Outline each Plasmodium malariae-infected red blood cell.
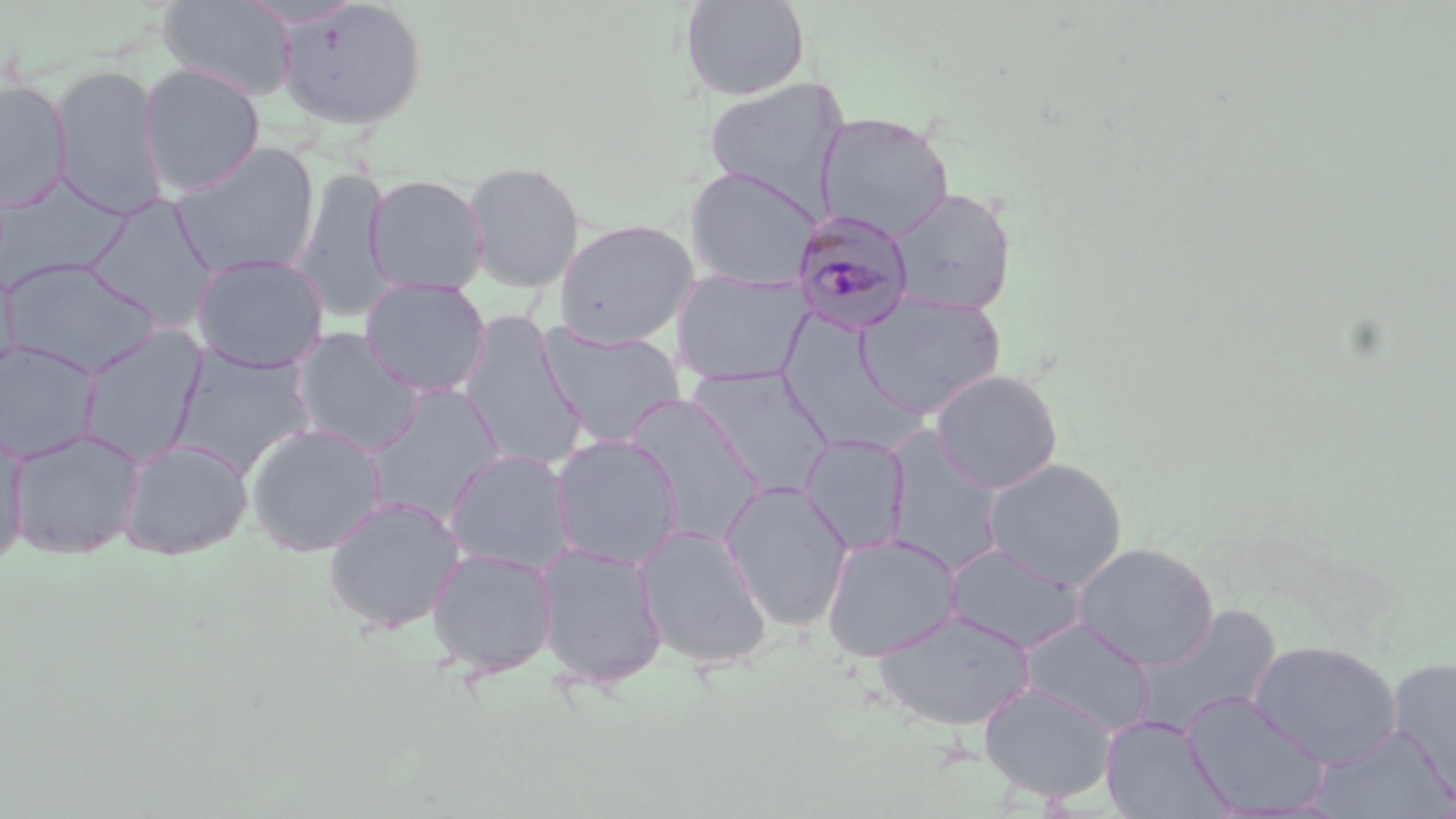
Approximate bounding boxes as [x1, y1, x2, y2] in pixels.
Plasmodium malariae-infected red blood cells: [790, 208, 916, 335].

Uninfected red blood cell locations: [158, 0, 296, 101], [276, 0, 428, 130], [680, 0, 810, 101], [138, 62, 265, 196], [50, 63, 168, 220], [0, 79, 72, 211], [702, 79, 849, 208], [815, 112, 954, 239], [170, 142, 321, 279], [462, 160, 586, 292], [684, 167, 822, 290], [293, 168, 395, 322], [365, 173, 489, 294], [0, 176, 129, 291], [887, 187, 1018, 317], [84, 194, 219, 330], [554, 219, 699, 349], [191, 253, 329, 373], [1, 257, 160, 376], [0, 262, 22, 383], [670, 267, 812, 388], [359, 278, 492, 397], [854, 291, 1005, 420], [458, 314, 589, 470], [538, 323, 686, 447], [77, 325, 207, 467], [290, 328, 425, 455], [0, 340, 102, 464], [170, 346, 316, 477], [687, 367, 835, 498], [930, 369, 1063, 493], [364, 386, 508, 522], [622, 393, 767, 544], [0, 422, 29, 565], [245, 422, 387, 557], [882, 427, 1006, 574], [7, 428, 144, 559], [551, 434, 684, 570], [800, 434, 911, 556], [118, 438, 253, 559], [444, 449, 576, 575], [982, 457, 1127, 590], [719, 481, 854, 629], [323, 495, 465, 634], [634, 524, 772, 669], [821, 532, 962, 662], [535, 540, 669, 690], [945, 542, 1086, 653], [1072, 543, 1219, 670], [426, 548, 558, 678], [1130, 605, 1282, 738], [873, 609, 1035, 732], [1019, 618, 1155, 736], [1248, 640, 1402, 767], [1387, 659, 1456, 797], [978, 681, 1117, 804], [1181, 691, 1331, 816], [1100, 715, 1230, 818], [1313, 725, 1454, 818]. Slide-level diagnosis: Plasmodium malariae. Captured at 1000x magnification. Image is 1456×819 pixels. May-Grünwald-Giemsa-stained preparation. Light microscopy. Single field of view. Thin blood film.